Report the malaria status of this cell.
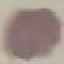

It is uninfected.

Acquired by smartphone through the microscope eyepiece. Giemsa stain. Thin blood smear. Automatically extracted cell patch, resized to 64 × 64 pixels.